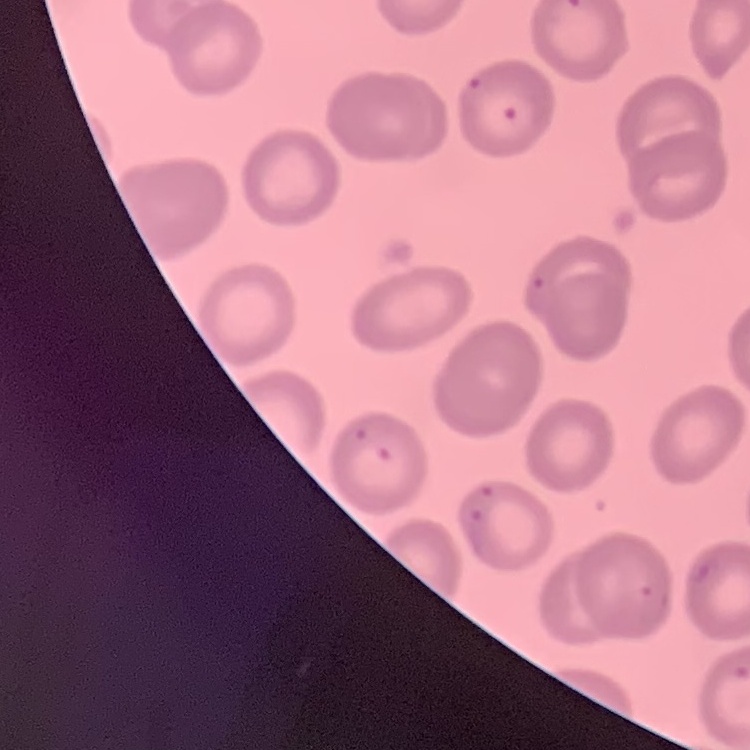

erythrocyte morphology = no rouleaux formation
stain = Field's or Giemsa
preparation = thin blood smear
image type = square crop of a larger photomicrograph